Comment on the morphology of the erythrocytes.
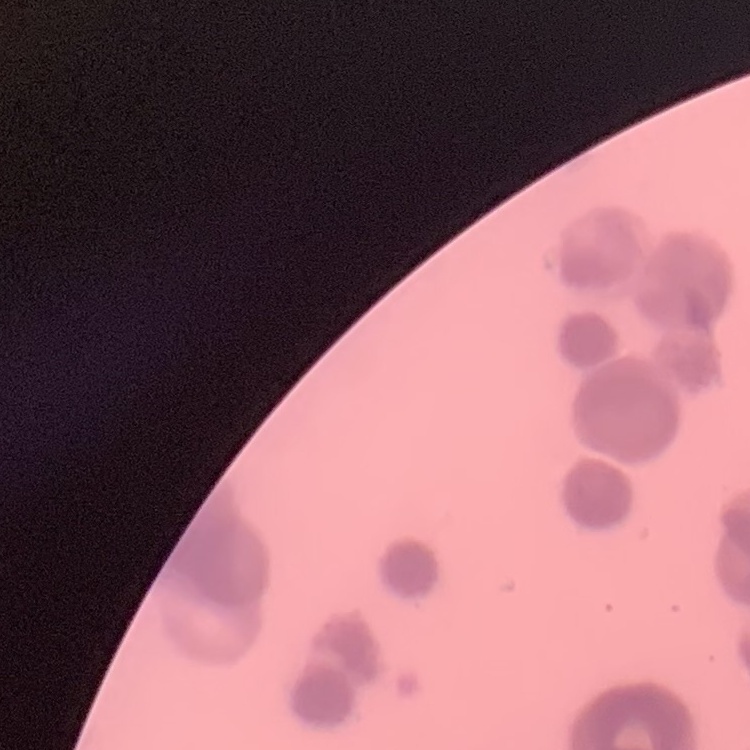
They show rouleaux formation.

Thin blood smear. One tile cut from a larger photomicrograph. Field's or Giemsa stain.